Comment on the morphology of the red blood cells.
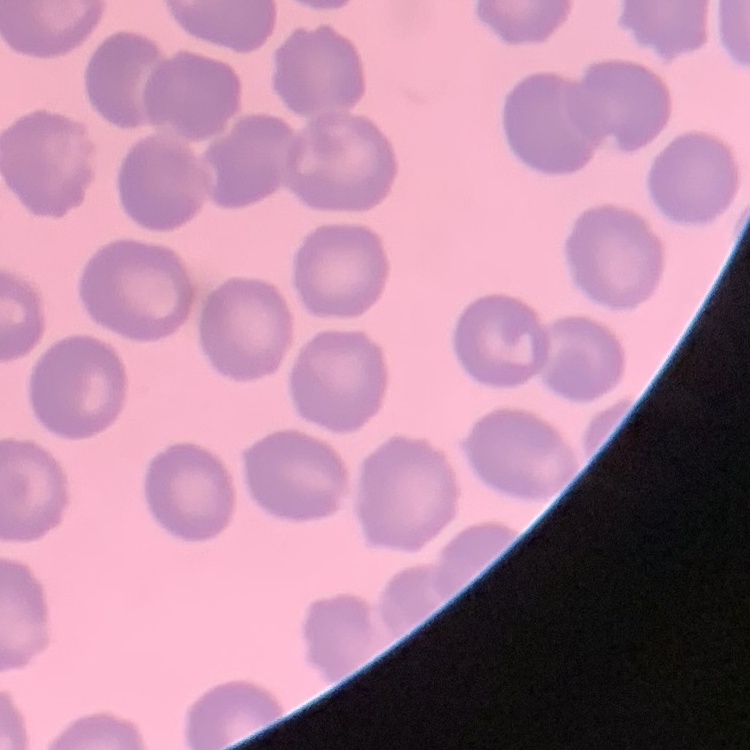
They show no rouleaux formation.

preparation = thin blood smear
image type = square crop of a larger photomicrograph
stain = Field's or Giemsa